Assess this cell for malaria.
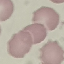

It is uninfected.

Acquired by smartphone through the microscope eyepiece. Cell patch, automatically extracted from a larger field of view and resized to 64 × 64 pixels. Thin blood film. Giemsa stain.